Name the cell type shown.
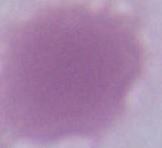
This is an erythrocyte.

Micrograph. Captured at 1000x magnification.